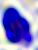
Summary:
  - Identification: white blood cell
  - Magnification: 400x
  - Modality: micrograph